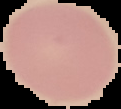

image_size: 121×109 pixels
preparation: thin blood smear
image_type: segmented cell region on a black background
result: no Plasmodium parasites detected